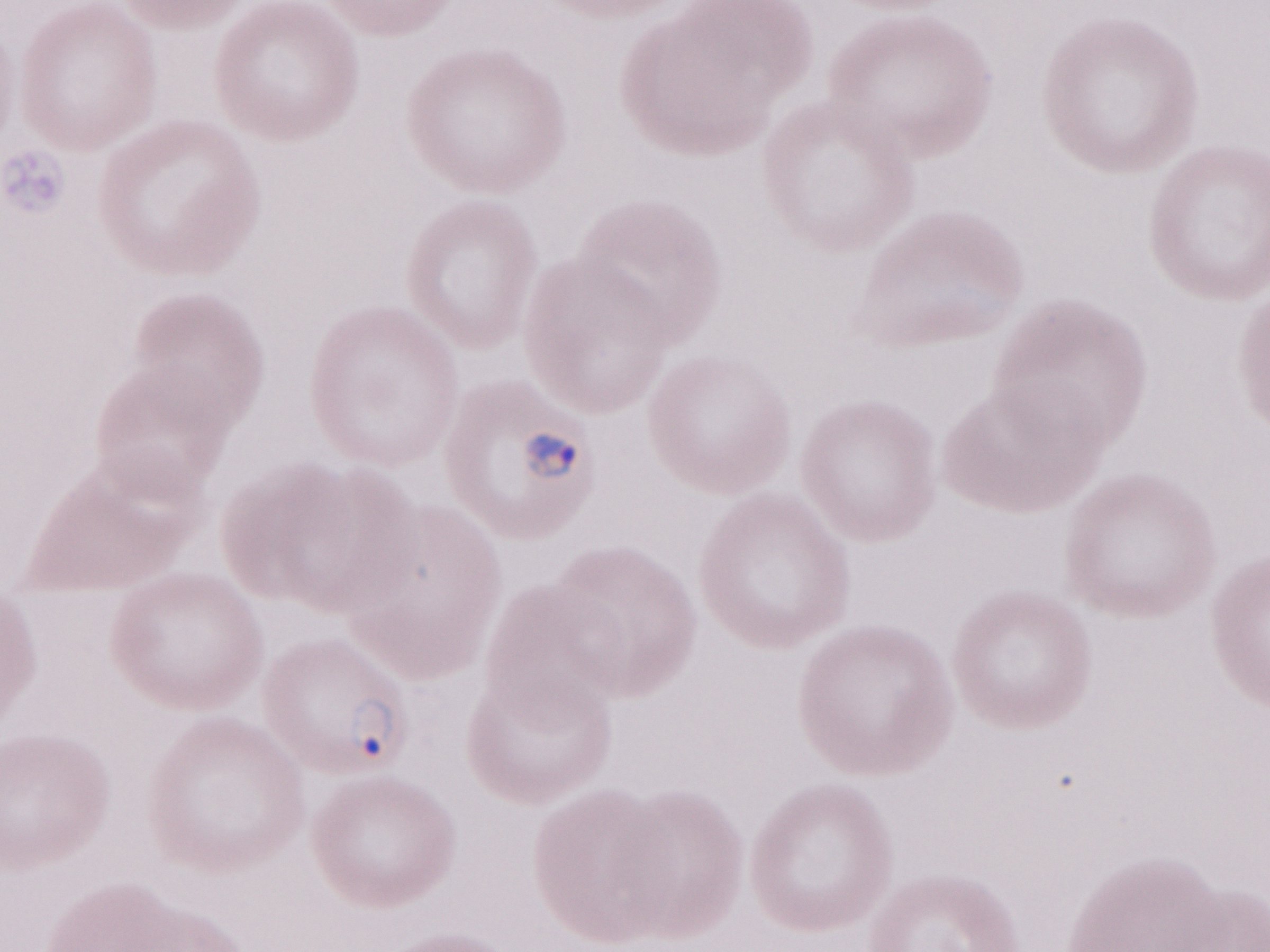
Olympus BX43 microscope and DP73 digital camera. Patient diagnosis: malaria infection. May-Grünwald-Giemsa-stained preparation. One field of this slide. 1,000x magnification. Image is 1270×952 pixels. Thin peripheral-blood smear.